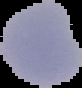

Summary:
  - Image type: segmented cell region with the area outside set to black
  - Image size: 82×88 pixels
  - Malaria status: parasitized
  - Preparation: thin blood smear